Outline each blood parasite and name the species.
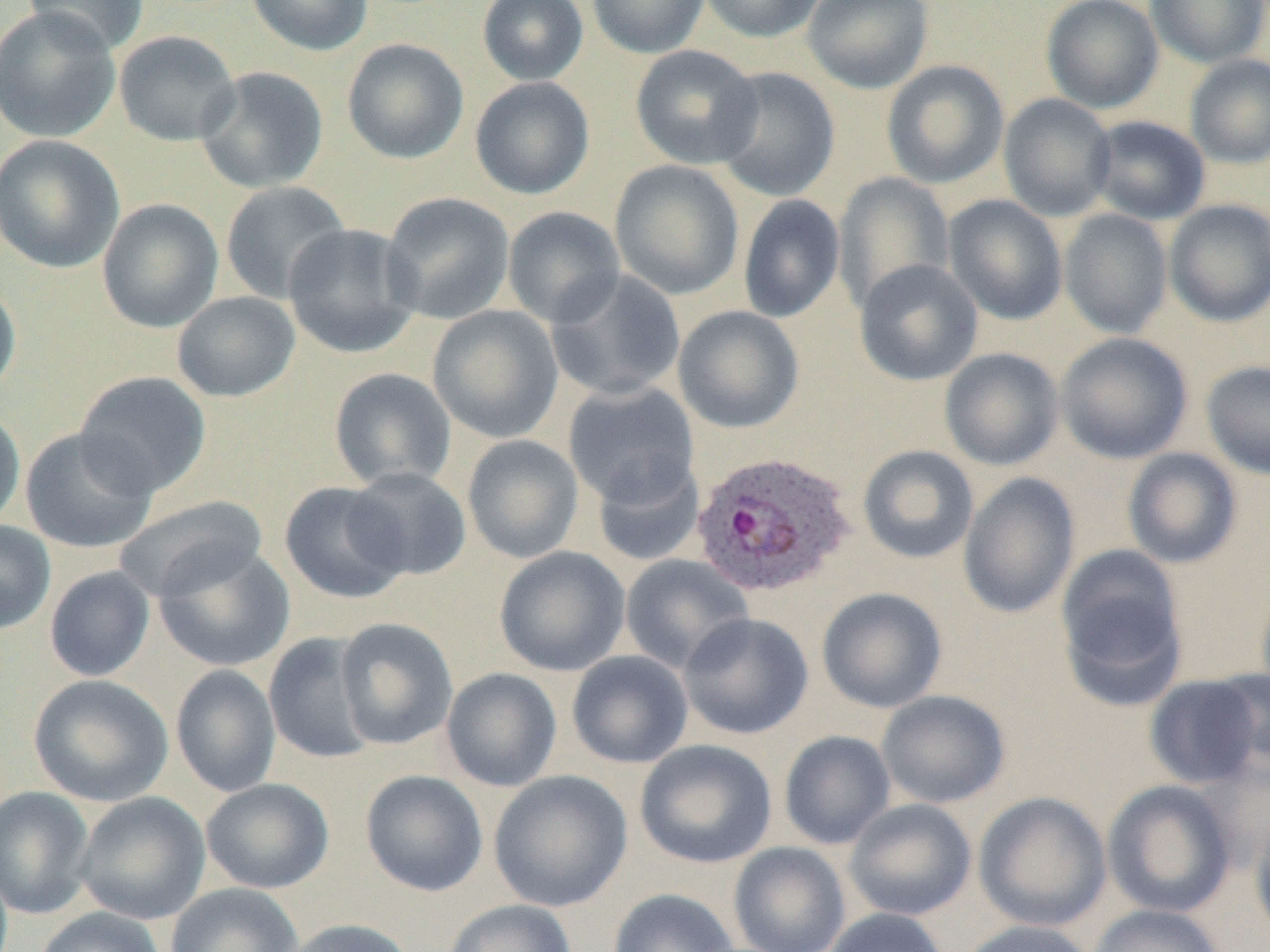

Approximate bounding boxes as (x1,y1)-(x2,y2) corner pairs in pixels.
Plasmodium ovale-infected red blood cells: (691,450)-(858,599).
No Plasmodium falciparum, Plasmodium malariae, Plasmodium vivax, Babesia divergens, or Trypanosoma brucei observed.

slide_level_diagnosis: Plasmodium ovale
preparation: thin blood film
field_of_view: one of a larger specimen
magnification: 1000x
modality: light microscopy
uninfected_red_blood_cell_locations: 'approximate bounding boxes as (x1,y1)-(x2,y2) corner pairs in pixels: (23,0)-(149,55), (244,0)-(374,56), (477,0)-(589,85), (587,0)-(709,58), (698,0)-(827,44), (801,0)-(934,94), (1041,0)-(1164,114), (1144,0)-(1270,67), (0,5)-(121,143), (114,30)-(241,146), (341,38)-(470,164), (630,44)-(762,169), (1185,54)-(1270,169), (881,60)-(1010,189), (195,66)-(328,193), (711,66)-(841,202), (470,76)-(595,199), (998,93)-(1118,222), (1088,116)-(1211,225), (0,134)-(124,273), (609,160)-(744,300), (832,172)-(955,314), (220,181)-(351,305), (380,192)-(515,325), (738,194)-(845,323), (942,194)-(1068,325), (97,199)-(224,333), (1164,200)-(1270,327), (502,206)-(625,328), (1059,209)-(1173,339), (283,223)-(423,358), (854,259)-(983,386), (545,268)-(687,402), (0,277)-(21,402), (171,291)-(300,402), (428,305)-(564,443), (672,305)-(804,434), (1055,332)-(1193,464), (939,347)-(1064,471), (1202,360)-(1270,480), (328,368)-(457,492), (74,371)-(211,497), (562,382)-(700,508), (0,405)-(25,532), (20,428)-(158,554), (462,435)-(584,564), (857,445)-(979,564), (1122,448)-(1243,569), (591,456)-(706,567), (344,466)-(472,582), (958,472)-(1080,619), (279,481)-(410,604), (112,495)-(267,603), (0,519)-(56,635), (153,544)-(295,671), (493,546)-(630,677), (1056,547)-(1188,706), (620,553)-(754,674), (44,566)-(156,682), (1255,578)-(1270,707), (817,587)-(948,714), (678,612)-(814,740), (334,617)-(458,750), (263,632)-(380,764), (566,650)-(693,769), (170,664)-(281,798), (440,667)-(562,792), (1209,670)-(1269,773), (28,674)-(173,808), (1144,674)-(1267,789), (876,689)-(1011,809), (779,730)-(896,850), (634,738)-(776,869), (360,769)-(488,897), (487,769)-(633,912), (200,778)-(335,893), (1102,780)-(1237,918), (0,786)-(95,920), (973,791)-(1112,932), (74,792)-(210,925), (843,798)-(977,921), (1249,809)-(1270,945), (728,842)-(851,952), (165,882)-(302,952), (607,888)-(740,952), (443,899)-(577,952), (1088,904)-(1227,952), (32,906)-(166,952), (821,908)-(949,952), (280,918)-(417,952), (956,920)-(1099,952)'
image_size: 1270×952 pixels